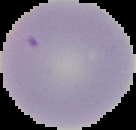
Summary:
  - Preparation: thin blood film
  - Malaria status: uninfected
  - Image type: segmented cell region with the area outside set to black
  - Image size: 136×130 pixels